Name the cell type shown.
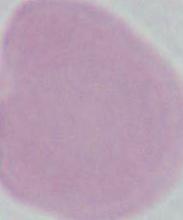
This is an erythrocyte.

Captured at 1000x magnification. Photomicrograph.